Name the blood parasite species.
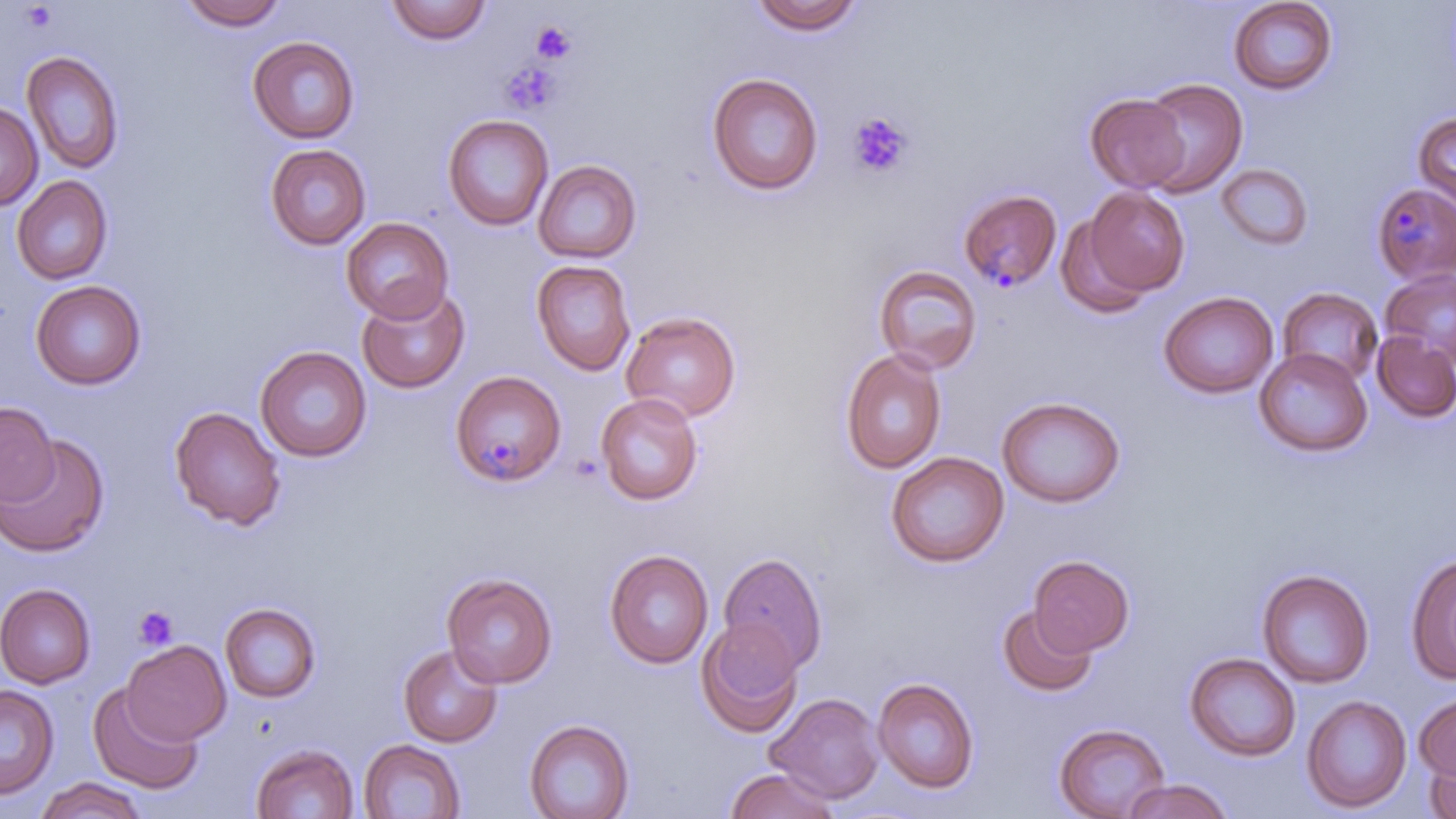
Plasmodium malariae.

Approximate bounding boxes as (x1, y1, x2, y2) in pixels. Uninfected red blood cell locations: (177, 0, 290, 30), (749, 0, 865, 35), (1227, 0, 1339, 95), (384, 1, 492, 45), (247, 36, 360, 144), (21, 50, 124, 175), (706, 72, 824, 196), (1137, 78, 1248, 197), (1085, 94, 1191, 192), (0, 102, 42, 210), (1413, 112, 1456, 214), (442, 114, 554, 231), (264, 144, 371, 250), (533, 159, 642, 264), (1217, 164, 1313, 250), (11, 175, 113, 285), (1083, 187, 1189, 298), (1053, 212, 1156, 319), (341, 217, 454, 324), (531, 259, 636, 376), (874, 264, 982, 375), (1380, 268, 1456, 367), (30, 280, 146, 389), (356, 284, 471, 394), (1278, 287, 1383, 386), (1158, 291, 1278, 399), (621, 311, 741, 423), (1372, 331, 1456, 423), (255, 345, 372, 462), (840, 348, 947, 474), (1254, 348, 1373, 457), (595, 392, 704, 505), (996, 395, 1126, 508), (0, 402, 59, 506), (169, 406, 286, 531), (0, 436, 109, 557), (886, 451, 1009, 568), (604, 548, 713, 668), (718, 551, 828, 674), (1405, 553, 1456, 686), (1029, 554, 1134, 656), (1256, 568, 1375, 688), (442, 571, 558, 687), (0, 583, 96, 689), (220, 602, 321, 703), (997, 605, 1097, 697), (696, 617, 803, 738), (122, 640, 231, 745), (396, 643, 503, 748), (1184, 652, 1301, 762), (872, 677, 980, 793), (88, 683, 203, 795), (0, 685, 59, 800), (766, 692, 885, 803), (1301, 694, 1413, 813), (1414, 694, 1456, 783), (524, 718, 634, 819), (1053, 722, 1171, 819), (359, 739, 467, 819), (251, 742, 359, 819), (1423, 749, 1456, 818), (725, 767, 841, 818), (35, 777, 146, 819), (1120, 778, 1233, 819). Platelet locations: (531, 20, 576, 64), (499, 61, 563, 116), (846, 112, 914, 179), (133, 606, 178, 651). Plasmodium malariae-infected red blood cell locations: (1371, 181, 1456, 284), (958, 188, 1062, 291), (451, 370, 566, 487). 1000x magnification. May-Grünwald-Giemsa-stained preparation. Single field of view. Image is 1456×819 pixels. Thin blood smear. Light microscopy.